Point out each Plasmodium parasite.
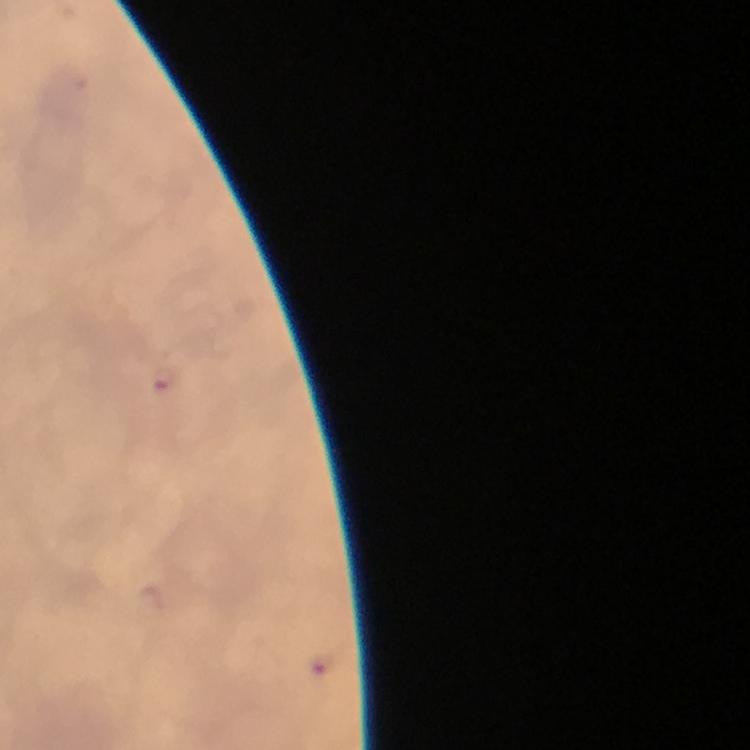
Approximate centers as {x, y} in pixels.
Plasmodium parasites: {165, 378}, {320, 662}.

Cropped region of a single field of view. From a diagnostic examination for malaria. Giemsa stain. At 100x magnification. Photographed through the microscope with a smartphone camera. Immersion oil applied. Image is 750×750 pixels. Thick blood smear.